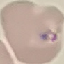 Result: negative for malaria parasites. Photographed with a smartphone camera at the microscope eyepiece. Automatically extracted cell patch, resized to 64 × 64 pixels. Thin smear of blood. Giemsa stain.